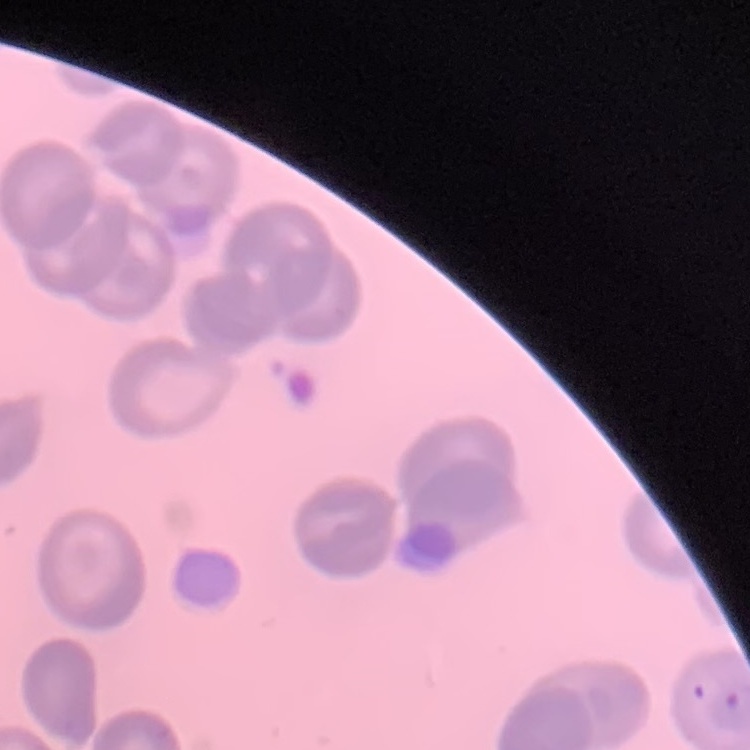
Summary:
  - Red blood cell morphology: no rouleaux formation
  - Preparation: thin blood smear
  - Image type: one tile cut from a larger photomicrograph
  - Stain: Field's or Giemsa